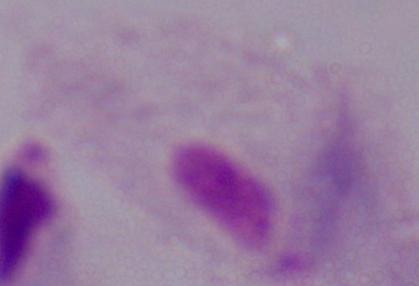

Micrograph. A trichomonad is seen. Captured at 1000x magnification.